Name the parasite shown.
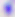
This is Toxoplasma gondii.

Captured at 400x magnification. Micrograph.